Assess the morphology of the erythrocytes.
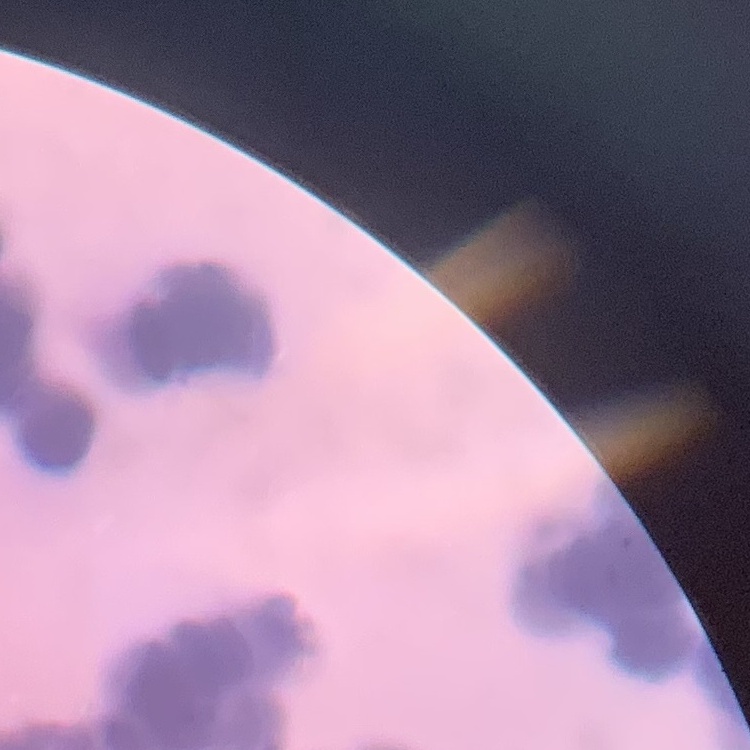

They show rouleaux formation.

image type = square crop of a larger photomicrograph
preparation = thin blood film
stain = Field's or Giemsa